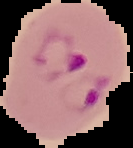

From a thin blood film. Image is 133×148 pixels. Cell region segmented out of the field of view; the surrounding area is masked to black. Result: malaria parasites identified.